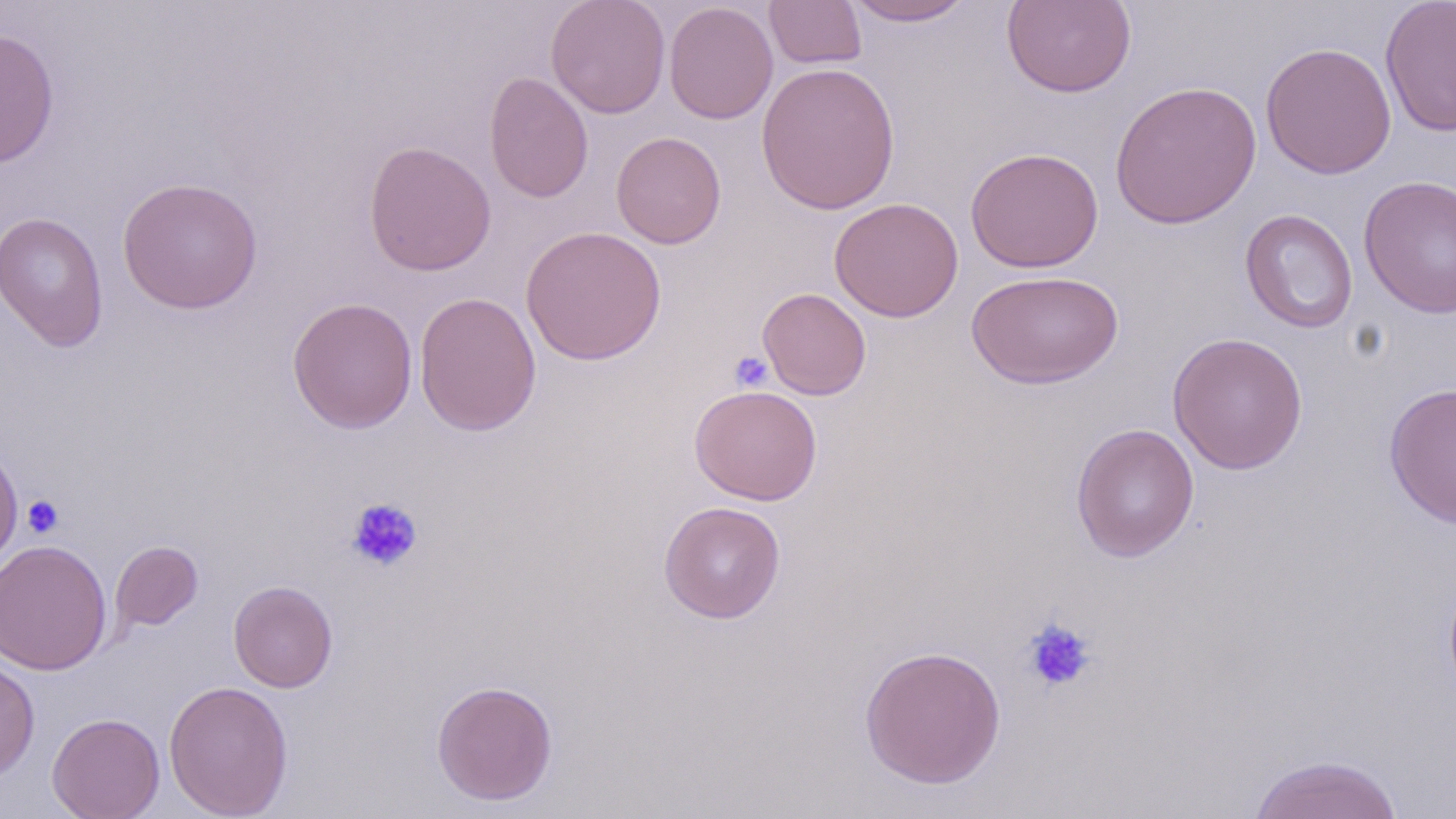
{
  "slide_level_diagnosis": "negative for blood parasites",
  "image_size": "1456×819 pixels",
  "stain": "May-Grünwald-Giemsa",
  "platelet_locations": "approximate bounding boxes as [x1, y1, x2, y2] in pixels: [729, 350, 774, 393], [21, 495, 64, 538], [345, 497, 423, 573], [1021, 617, 1097, 693]",
  "modality": "optical microscopy",
  "uninfected_red_blood_cell_locations": "approximate bounding boxes as [x1, y1, x2, y2] in pixels: [545, 0, 671, 118], [764, 0, 867, 69], [844, 0, 975, 26], [1001, 0, 1137, 98], [1380, 0, 1456, 138], [663, 2, 778, 124], [0, 27, 59, 169], [1260, 41, 1397, 180], [756, 62, 900, 215], [483, 71, 594, 204], [1110, 80, 1263, 230], [611, 132, 727, 249], [363, 140, 496, 276], [965, 146, 1104, 273], [1359, 175, 1456, 319], [116, 176, 264, 314], [828, 197, 964, 322], [1240, 209, 1359, 334], [0, 211, 110, 352], [521, 225, 667, 365], [966, 269, 1124, 389], [757, 287, 872, 400], [414, 291, 542, 436], [287, 296, 418, 434], [1167, 332, 1308, 474], [1384, 380, 1456, 530], [689, 384, 822, 505], [1070, 422, 1200, 563], [0, 439, 23, 571], [658, 501, 786, 624], [0, 540, 113, 675], [110, 541, 203, 632], [228, 580, 338, 693], [859, 643, 1007, 789], [0, 656, 40, 781], [163, 679, 294, 819], [431, 680, 558, 805], [47, 712, 165, 819], [1247, 753, 1405, 818]",
  "preparation": "thin blood film",
  "magnification": "1000x",
  "field_of_view": "one of a larger specimen"
}